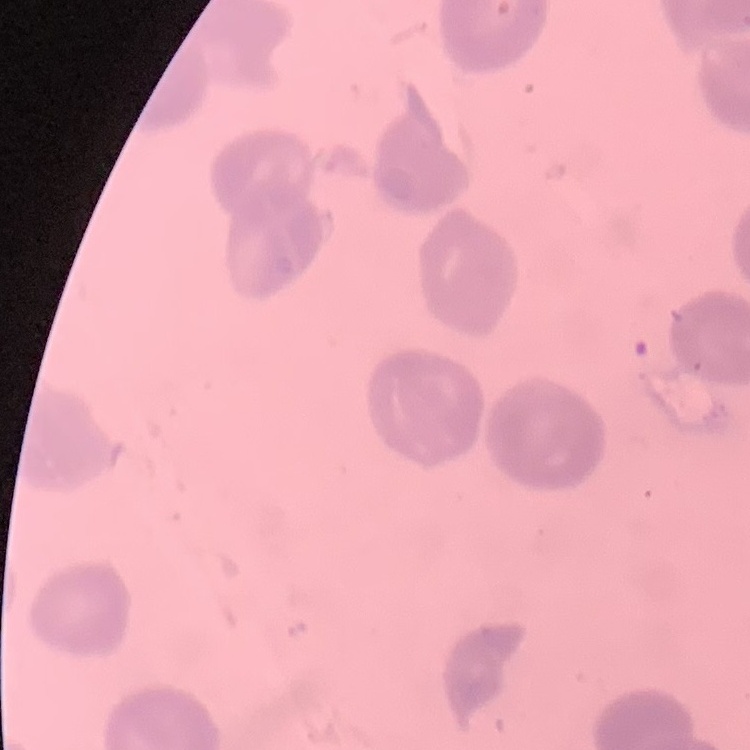 The erythrocytes exhibit no rouleaux formation. Square crop of a larger photomicrograph. Stained with either Field's or Giemsa. Thin blood smear.